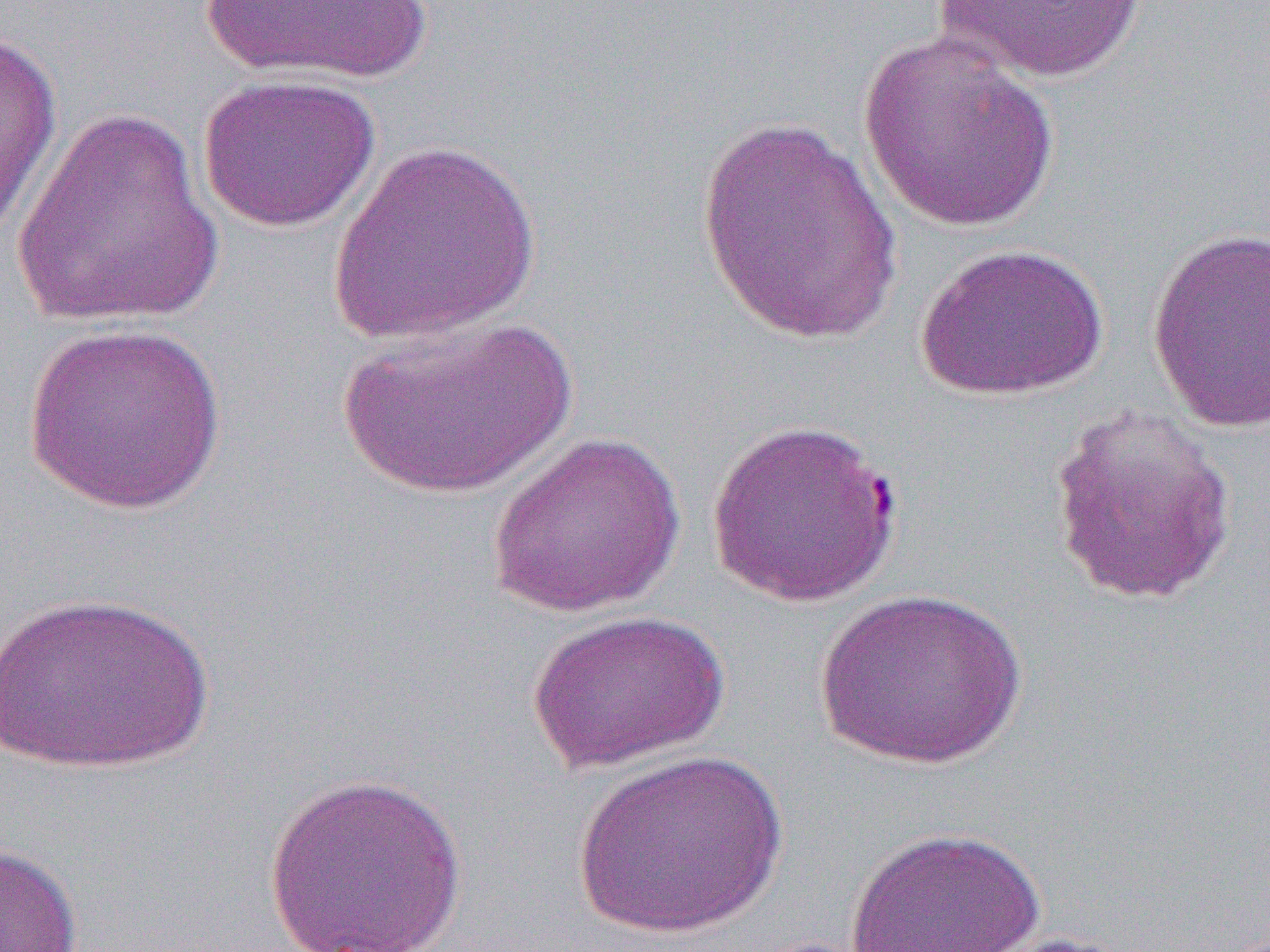
Approximate bounding boxes as (x1,y1)-(x2,y2) corner pairs in pixels. Uninfected red blood cell locations: (198,0)-(435,84), (929,0)-(1153,84), (0,23)-(63,252), (857,33)-(1061,234), (198,73)-(381,233), (11,107)-(227,329), (693,115)-(909,348), (326,140)-(543,346), (1146,227)-(1270,433), (914,242)-(1111,401), (334,316)-(577,501), (22,321)-(227,516), (1045,402)-(1239,607), (707,417)-(907,610), (487,431)-(687,619), (813,588)-(1029,770), (0,590)-(215,774), (525,609)-(730,774), (570,748)-(788,941), (263,771)-(468,951), (844,827)-(1047,951), (0,842)-(84,951), (975,931)-(1142,952). Slide-level diagnosis: Plasmodium falciparum. Thin blood smear. Image is 1270×952 pixels. Optical microscopy. 1000x magnification. One field of a larger specimen.